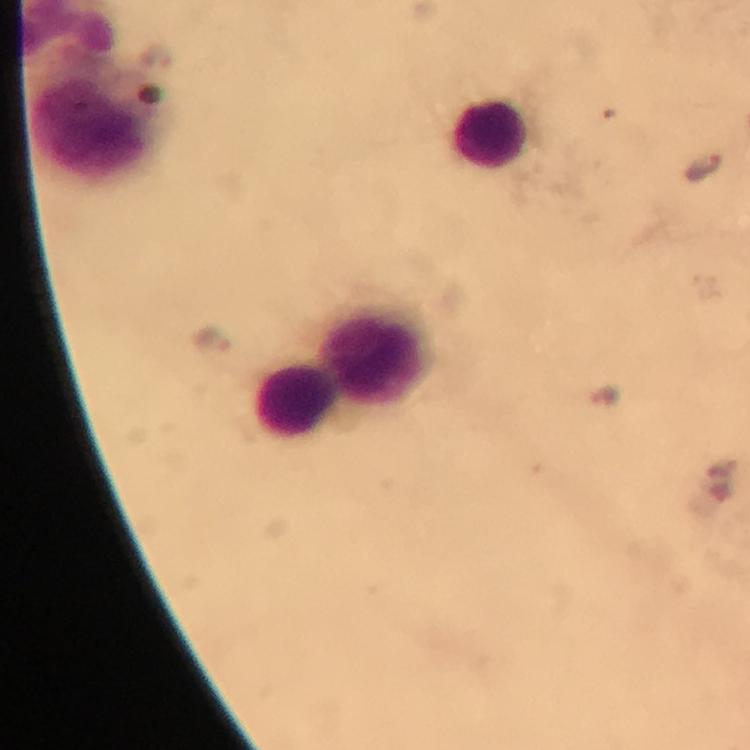

{
  "immersion_oil": "used",
  "cropped_from": "a single field of view",
  "plasmodium_parasite_locations": "approximate centers as {x, y} in pixels: {706, 169}, {212, 339}, {604, 396}",
  "image_size": "750×750 pixels",
  "context": "from a diagnostic examination for malaria",
  "stain": "Giemsa",
  "capture": "smartphone camera through the microscope",
  "magnification": "100x",
  "leukocyte_locations": "approximate centers as {x, y} in pixels: {491, 133}, {375, 352}, {298, 400}",
  "preparation": "thick blood film"
}